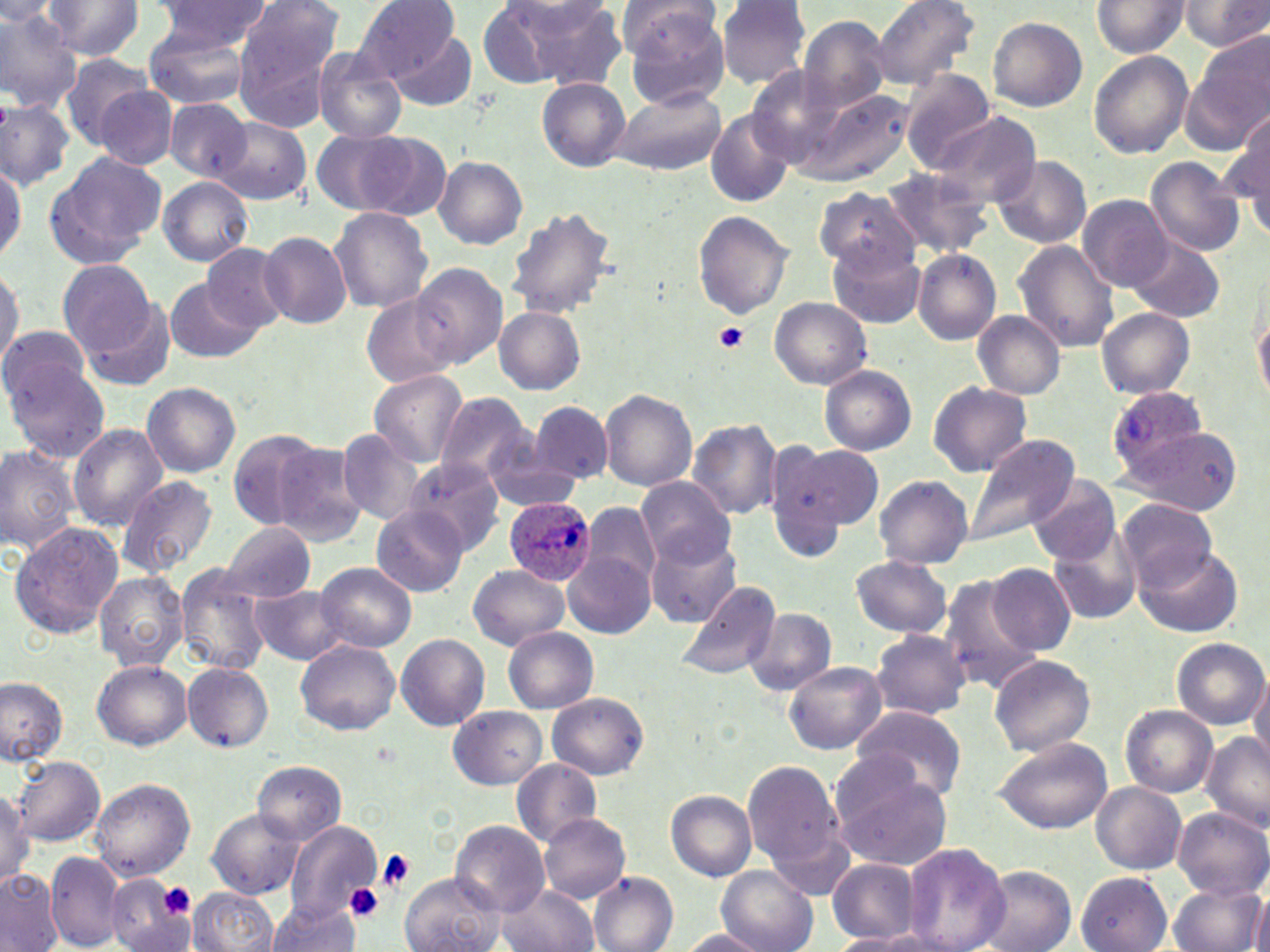

Summary:
  - Coordinate format: approximate bounding boxes as named x1/y1/x2/y2 corners in pixels
  - Platelet locations: (x1=714, y1=322, x2=750, y2=354), (x1=376, y1=850, x2=416, y2=891), (x1=157, y1=882, x2=196, y2=919), (x1=345, y1=884, x2=383, y2=921)
  - Plasmodium ovale-infected red blood cell locations: (x1=1106, y1=384, x2=1210, y2=478), (x1=504, y1=497, x2=595, y2=585)
  - Uninfected red blood cell locations: (x1=153, y1=0, x2=273, y2=53), (x1=351, y1=0, x2=463, y2=81), (x1=716, y1=0, x2=812, y2=88), (x1=871, y1=0, x2=980, y2=90), (x1=39, y1=1, x2=145, y2=60), (x1=238, y1=1, x2=346, y2=89), (x1=1090, y1=1, x2=1190, y2=57), (x1=1178, y1=1, x2=1270, y2=51), (x1=0, y1=2, x2=58, y2=25), (x1=515, y1=2, x2=631, y2=91), (x1=623, y1=4, x2=730, y2=109), (x1=0, y1=9, x2=83, y2=112), (x1=989, y1=16, x2=1087, y2=112), (x1=798, y1=17, x2=891, y2=113), (x1=142, y1=24, x2=252, y2=109), (x1=392, y1=30, x2=477, y2=112), (x1=1192, y1=31, x2=1270, y2=143), (x1=313, y1=49, x2=407, y2=142), (x1=1088, y1=51, x2=1193, y2=158), (x1=60, y1=57, x2=160, y2=150), (x1=746, y1=66, x2=855, y2=167), (x1=900, y1=70, x2=995, y2=173), (x1=537, y1=78, x2=630, y2=171), (x1=95, y1=86, x2=178, y2=170), (x1=609, y1=88, x2=725, y2=176), (x1=803, y1=89, x2=908, y2=183), (x1=0, y1=97, x2=74, y2=189), (x1=166, y1=98, x2=252, y2=181), (x1=1232, y1=108, x2=1269, y2=198), (x1=706, y1=110, x2=793, y2=208), (x1=928, y1=113, x2=1041, y2=210), (x1=213, y1=117, x2=311, y2=206), (x1=310, y1=127, x2=438, y2=219), (x1=1238, y1=139, x2=1270, y2=241), (x1=46, y1=151, x2=165, y2=265), (x1=992, y1=155, x2=1091, y2=248), (x1=433, y1=156, x2=527, y2=248), (x1=1145, y1=157, x2=1246, y2=256), (x1=0, y1=161, x2=25, y2=264), (x1=879, y1=167, x2=989, y2=260), (x1=158, y1=177, x2=254, y2=266), (x1=812, y1=187, x2=920, y2=272), (x1=1078, y1=193, x2=1173, y2=291), (x1=507, y1=206, x2=619, y2=317), (x1=327, y1=207, x2=434, y2=312), (x1=1041, y1=207, x2=1140, y2=321), (x1=693, y1=211, x2=794, y2=317), (x1=259, y1=231, x2=351, y2=328), (x1=1127, y1=236, x2=1224, y2=323), (x1=1013, y1=241, x2=1119, y2=351), (x1=830, y1=242, x2=926, y2=329), (x1=202, y1=244, x2=291, y2=332), (x1=912, y1=249, x2=1001, y2=344), (x1=57, y1=258, x2=158, y2=362), (x1=410, y1=263, x2=507, y2=367), (x1=0, y1=265, x2=22, y2=369), (x1=165, y1=278, x2=261, y2=363), (x1=72, y1=292, x2=177, y2=393), (x1=362, y1=294, x2=459, y2=387), (x1=770, y1=297, x2=871, y2=388), (x1=1253, y1=306, x2=1270, y2=405), (x1=1095, y1=307, x2=1196, y2=398), (x1=494, y1=308, x2=585, y2=393), (x1=973, y1=312, x2=1066, y2=399), (x1=0, y1=324, x2=94, y2=412), (x1=7, y1=363, x2=111, y2=463), (x1=820, y1=365, x2=917, y2=456), (x1=369, y1=368, x2=467, y2=467), (x1=929, y1=381, x2=1031, y2=477), (x1=141, y1=382, x2=240, y2=478), (x1=601, y1=389, x2=697, y2=491), (x1=433, y1=391, x2=535, y2=487), (x1=530, y1=400, x2=613, y2=485), (x1=688, y1=418, x2=784, y2=520), (x1=68, y1=423, x2=168, y2=529), (x1=1122, y1=426, x2=1242, y2=516), (x1=226, y1=429, x2=332, y2=528), (x1=337, y1=430, x2=423, y2=525), (x1=962, y1=433, x2=1079, y2=546), (x1=270, y1=441, x2=369, y2=546), (x1=0, y1=442, x2=81, y2=555), (x1=775, y1=442, x2=884, y2=534), (x1=485, y1=450, x2=582, y2=512), (x1=401, y1=459, x2=505, y2=554), (x1=116, y1=475, x2=218, y2=578), (x1=874, y1=475, x2=973, y2=570), (x1=1028, y1=475, x2=1120, y2=565), (x1=636, y1=476, x2=734, y2=568), (x1=1118, y1=500, x2=1219, y2=591), (x1=582, y1=503, x2=659, y2=595), (x1=372, y1=505, x2=468, y2=596), (x1=9, y1=522, x2=124, y2=640), (x1=219, y1=522, x2=317, y2=604), (x1=1050, y1=531, x2=1144, y2=627), (x1=646, y1=532, x2=741, y2=628), (x1=1136, y1=544, x2=1241, y2=638), (x1=564, y1=554, x2=652, y2=638), (x1=850, y1=555, x2=953, y2=638), (x1=316, y1=562, x2=416, y2=651), (x1=987, y1=563, x2=1075, y2=655), (x1=467, y1=564, x2=568, y2=650), (x1=175, y1=565, x2=274, y2=676), (x1=94, y1=571, x2=189, y2=672), (x1=937, y1=573, x2=1043, y2=693), (x1=675, y1=580, x2=780, y2=682), (x1=251, y1=585, x2=349, y2=664), (x1=743, y1=608, x2=836, y2=697), (x1=503, y1=628, x2=597, y2=712), (x1=870, y1=628, x2=971, y2=720), (x1=395, y1=633, x2=490, y2=730), (x1=1171, y1=638, x2=1267, y2=728), (x1=296, y1=640, x2=400, y2=737), (x1=989, y1=654, x2=1096, y2=757), (x1=91, y1=659, x2=192, y2=751), (x1=786, y1=662, x2=887, y2=754), (x1=182, y1=663, x2=273, y2=752), (x1=1249, y1=672, x2=1270, y2=767), (x1=0, y1=675, x2=69, y2=765), (x1=547, y1=693, x2=648, y2=779), (x1=851, y1=704, x2=967, y2=800), (x1=1122, y1=705, x2=1216, y2=798), (x1=448, y1=706, x2=546, y2=789), (x1=1201, y1=732, x2=1270, y2=831), (x1=991, y1=737, x2=1113, y2=834), (x1=11, y1=755, x2=104, y2=846), (x1=829, y1=757, x2=953, y2=870), (x1=741, y1=759, x2=845, y2=881), (x1=251, y1=760, x2=346, y2=843), (x1=511, y1=760, x2=602, y2=847), (x1=90, y1=777, x2=196, y2=882), (x1=1091, y1=782, x2=1186, y2=874), (x1=0, y1=787, x2=33, y2=887), (x1=666, y1=790, x2=757, y2=881), (x1=1089, y1=796, x2=1270, y2=883), (x1=205, y1=808, x2=306, y2=900), (x1=1173, y1=809, x2=1270, y2=899), (x1=539, y1=813, x2=631, y2=904), (x1=286, y1=821, x2=382, y2=921), (x1=450, y1=821, x2=550, y2=916), (x1=900, y1=843, x2=1011, y2=952), (x1=46, y1=850, x2=127, y2=949), (x1=826, y1=858, x2=920, y2=942), (x1=975, y1=866, x2=1077, y2=952), (x1=717, y1=868, x2=816, y2=952), (x1=0, y1=869, x2=64, y2=952), (x1=398, y1=871, x2=504, y2=952), (x1=588, y1=871, x2=678, y2=952), (x1=1075, y1=872, x2=1173, y2=951), (x1=107, y1=878, x2=194, y2=951), (x1=1167, y1=880, x2=1265, y2=952), (x1=496, y1=885, x2=599, y2=952), (x1=189, y1=886, x2=279, y2=952), (x1=1252, y1=895, x2=1270, y2=952), (x1=266, y1=899, x2=360, y2=952), (x1=676, y1=929, x2=770, y2=950), (x1=829, y1=932, x2=933, y2=951)
  - Slide-level diagnosis: Plasmodium ovale
  - Field of view: single
  - Magnification: 1000x
  - Preparation: thin blood smear
  - Modality: light microscopy
  - Image size: 1270×952 pixels
  - Stain: May-Grünwald-Giemsa